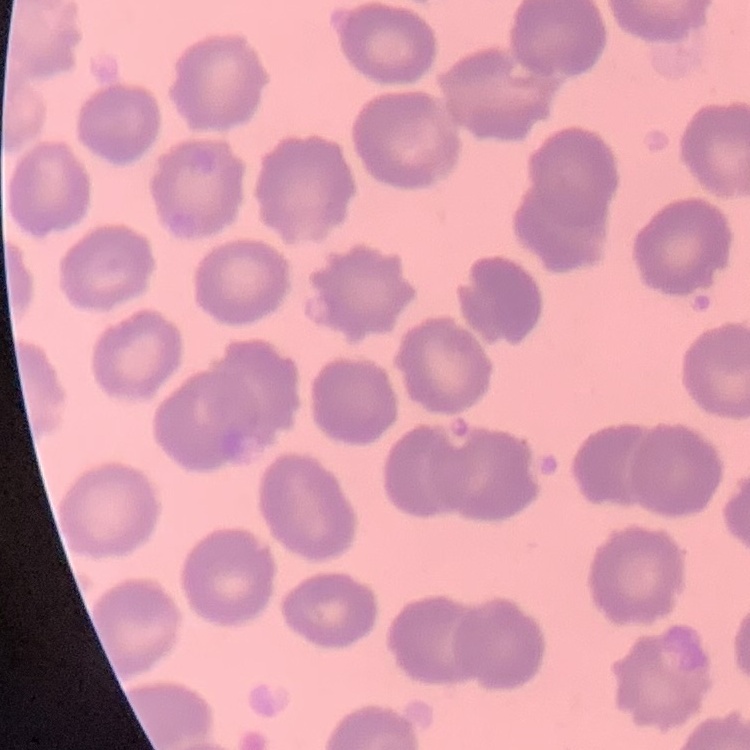
erythrocyte morphology = no rouleaux formation
image type = one tile cut from a larger photomicrograph
stain = Field's or Giemsa
preparation = thin peripheral smear